Outline each blood parasite and name the species.
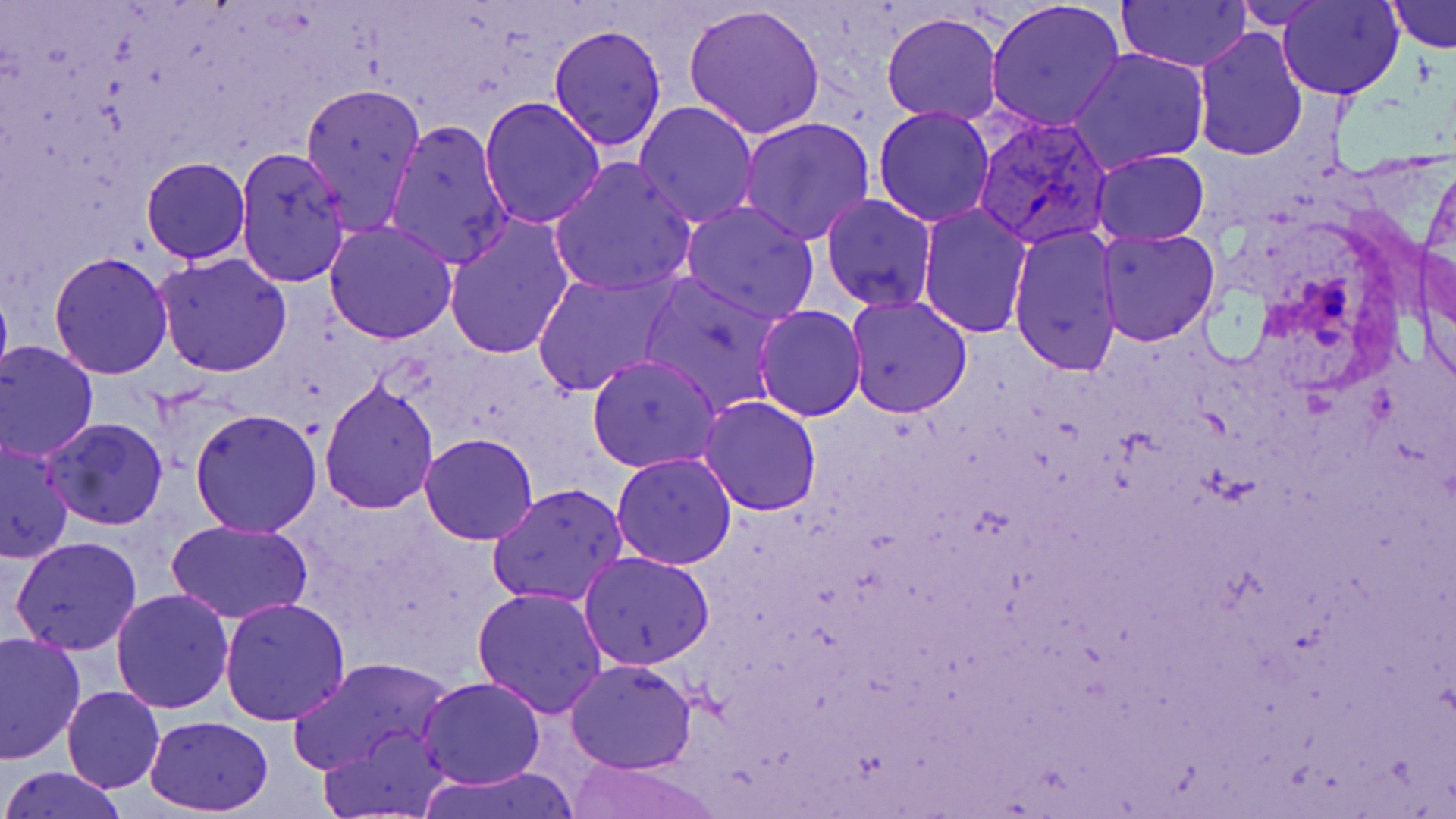

Approximate bounding boxes as (x1, y1, x2, y2) in pixels.
Plasmodium vivax-infected red blood cells: (972, 115, 1113, 251).
No Plasmodium falciparum, Plasmodium ovale, Plasmodium malariae, Babesia divergens, or Trypanosoma brucei observed.

Uninfected red blood cell locations: (985, 0, 1125, 133), (1233, 0, 1335, 27), (1278, 0, 1404, 100), (1388, 0, 1455, 50), (1118, 1, 1252, 72), (682, 2, 827, 141), (880, 10, 1004, 126), (550, 25, 667, 150), (1191, 25, 1308, 162), (1068, 48, 1208, 173), (299, 80, 426, 236), (476, 96, 606, 228), (633, 101, 761, 229), (872, 105, 997, 226), (738, 116, 878, 246), (383, 119, 513, 269), (234, 144, 351, 292), (1090, 150, 1211, 245), (140, 156, 251, 263), (547, 156, 698, 299), (820, 194, 938, 312), (679, 200, 820, 323), (917, 205, 1031, 339), (442, 212, 575, 359), (323, 218, 458, 344), (1007, 225, 1122, 378), (1095, 227, 1222, 346), (1420, 247, 1456, 393), (48, 250, 175, 379), (154, 251, 293, 377), (532, 265, 680, 398), (639, 271, 784, 417), (0, 281, 13, 392), (845, 294, 973, 418), (754, 305, 867, 421), (0, 340, 99, 461), (587, 354, 720, 473), (318, 377, 439, 512), (698, 396, 820, 515), (190, 409, 324, 538), (40, 419, 167, 532), (420, 433, 538, 545), (0, 440, 73, 563), (611, 452, 738, 570), (448, 457, 590, 592), (486, 484, 628, 609), (166, 519, 313, 624), (10, 535, 143, 656), (577, 552, 716, 671), (472, 587, 609, 719), (111, 589, 235, 713), (219, 595, 350, 725), (0, 630, 85, 762), (284, 655, 456, 776), (565, 658, 697, 772), (418, 675, 546, 789), (61, 685, 164, 794), (143, 714, 273, 816), (320, 723, 451, 818), (564, 758, 716, 819), (1, 766, 125, 819), (422, 767, 583, 819). Slide-level diagnosis: Plasmodium vivax. Image is 1456×819 pixels. Thin blood smear. One field of a larger specimen. Light microscopy. 1000x magnification. May-Grünwald-Giemsa-stained preparation.